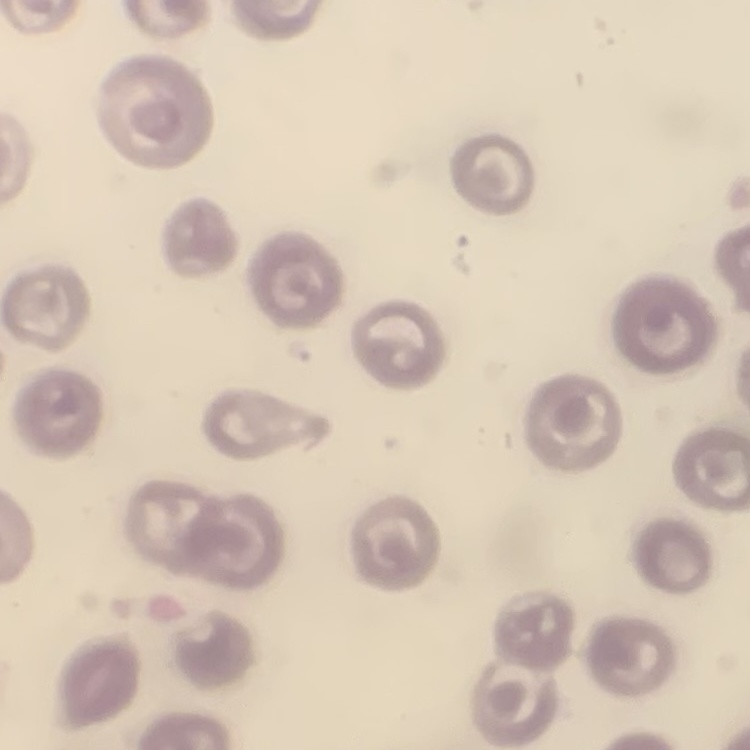

The red blood cells exhibit no rouleaux formation. One tile cut from a larger photomicrograph. Stained with either Field's or Giemsa. Thin peripheral smear.